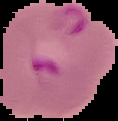
image type = cell region segmented out of the field of view; surrounding area masked to black
result = malaria parasites detected
preparation = thin blood smear
image size = 118×121 pixels